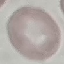
Summary:
  - Result: no malaria parasites detected
  - Preparation: thin blood film
  - Capture: smartphone through the microscope eyepiece
  - Image type: automatically extracted cell patch, resized to 64 × 64 pixels
  - Stain: Giemsa